Point out Plasmodium parasites and leukocytes.
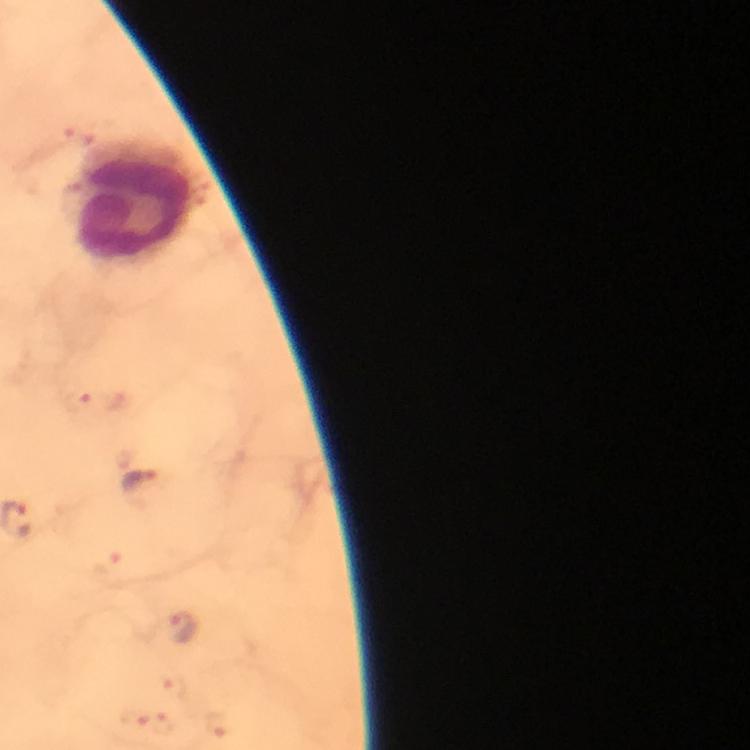

Approximate centers as {x, y} in pixels.
Plasmodium parasites: {141, 480}, {186, 630}.
Leukocytes: {134, 201}.

At 100x magnification. Immersion oil applied. Image is 750×750 pixels. Giemsa-stained preparation. From a malaria diagnostic workup. Thick smear. Photographed with a smartphone mounted on the microscope. A crop from one field of view.